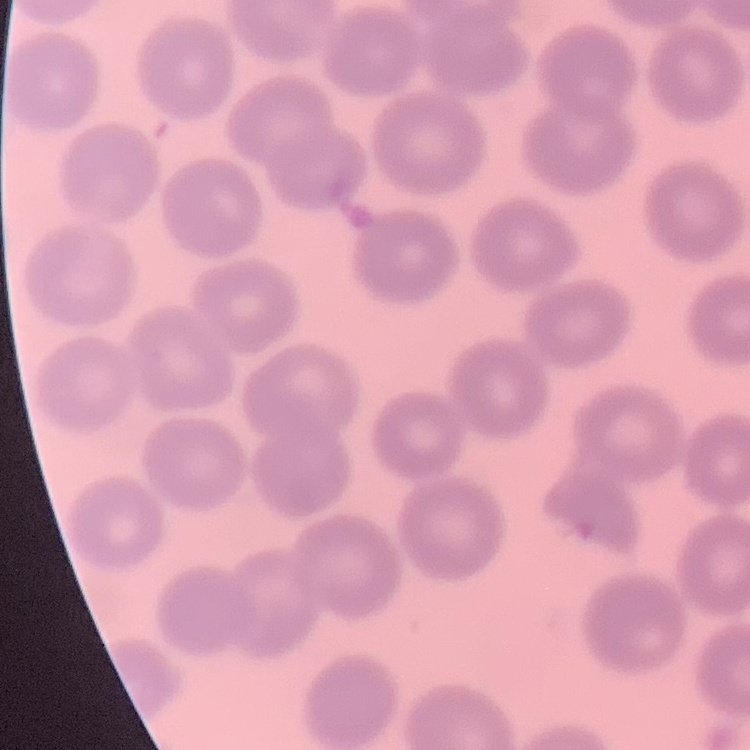
red blood cell morphology = no rouleaux formation
preparation = thin blood film
stain = Field's or Giemsa
image type = one tile cut from a larger photomicrograph